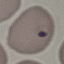
{
  "result": "malaria parasites identified",
  "stain": "Giemsa",
  "image_type": "automatically extracted cell patch, resized to 64 × 64 pixels",
  "preparation": "thin blood film",
  "capture": "smartphone through the microscope eyepiece"
}